State the blood parasite species.
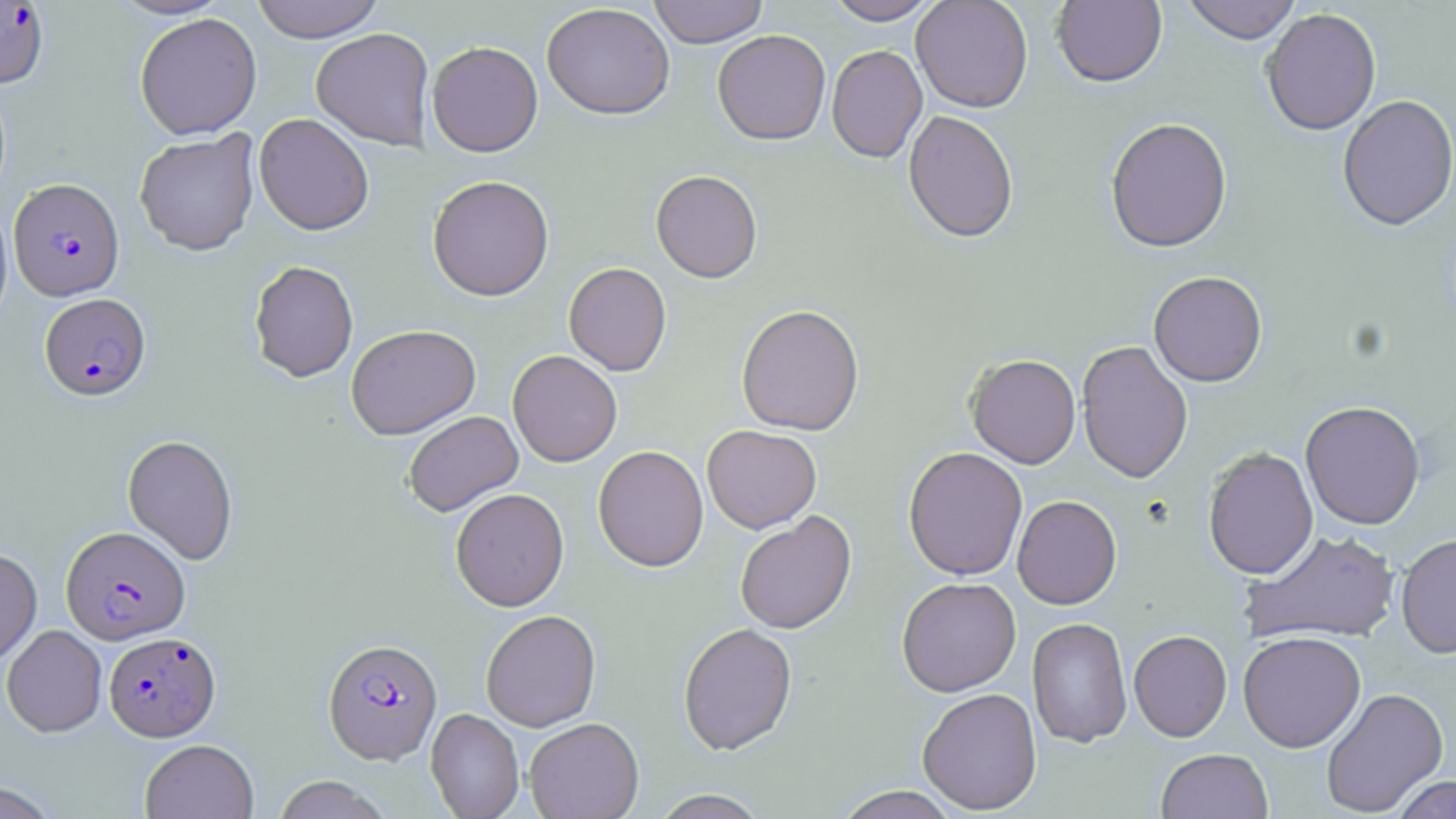

Plasmodium falciparum.

field_of_view: one of a larger specimen
stain: May-Grünwald-Giemsa
modality: light microscopy
preparation: thin blood smear
plasmodium_falciparum_infected_red_blood_cell_locations: 'approximate bounding boxes as named x1/y1/x2/y2 corners in pixels: (x1=0, y1=1, x2=50, y2=88), (x1=8, y1=178, x2=125, y2=300), (x1=39, y1=293, x2=151, y2=400), (x1=61, y1=525, x2=190, y2=644), (x1=104, y1=631, x2=220, y2=741), (x1=323, y1=638, x2=442, y2=764)'
image_size: 1456×819 pixels
uninfected_red_blood_cell_locations: 'approximate bounding boxes as named x1/y1/x2/y2 corners in pixels: (x1=109, y1=0, x2=232, y2=20), (x1=251, y1=0, x2=385, y2=43), (x1=648, y1=0, x2=768, y2=48), (x1=825, y1=0, x2=941, y2=25), (x1=911, y1=0, x2=1033, y2=114), (x1=1051, y1=0, x2=1167, y2=88), (x1=1181, y1=0, x2=1303, y2=45), (x1=541, y1=2, x2=675, y2=120), (x1=1261, y1=9, x2=1382, y2=137), (x1=134, y1=12, x2=262, y2=140), (x1=310, y1=27, x2=434, y2=151), (x1=712, y1=29, x2=831, y2=146), (x1=426, y1=41, x2=543, y2=157), (x1=826, y1=45, x2=927, y2=163), (x1=1337, y1=96, x2=1456, y2=233), (x1=903, y1=110, x2=1019, y2=244), (x1=254, y1=113, x2=374, y2=235), (x1=1105, y1=119, x2=1232, y2=255), (x1=134, y1=130, x2=260, y2=256), (x1=651, y1=169, x2=763, y2=283), (x1=427, y1=174, x2=555, y2=301), (x1=0, y1=198, x2=14, y2=333), (x1=248, y1=260, x2=359, y2=382), (x1=564, y1=262, x2=672, y2=376), (x1=1148, y1=272, x2=1268, y2=387), (x1=736, y1=304, x2=864, y2=436), (x1=345, y1=324, x2=481, y2=439), (x1=1076, y1=340, x2=1193, y2=484), (x1=507, y1=350, x2=622, y2=467), (x1=966, y1=355, x2=1081, y2=469), (x1=1300, y1=401, x2=1425, y2=530), (x1=403, y1=410, x2=523, y2=517), (x1=702, y1=424, x2=822, y2=533), (x1=122, y1=434, x2=239, y2=564), (x1=593, y1=445, x2=708, y2=572), (x1=903, y1=447, x2=1028, y2=581), (x1=1203, y1=447, x2=1318, y2=580), (x1=450, y1=487, x2=569, y2=611), (x1=1012, y1=495, x2=1122, y2=610), (x1=735, y1=512, x2=856, y2=634), (x1=1240, y1=528, x2=1401, y2=647), (x1=1396, y1=533, x2=1455, y2=659), (x1=0, y1=549, x2=42, y2=666), (x1=896, y1=577, x2=1021, y2=697), (x1=481, y1=610, x2=601, y2=731), (x1=1027, y1=617, x2=1133, y2=748), (x1=678, y1=623, x2=798, y2=755), (x1=1, y1=625, x2=107, y2=737), (x1=1129, y1=630, x2=1232, y2=742), (x1=1237, y1=631, x2=1366, y2=752), (x1=917, y1=687, x2=1042, y2=815), (x1=1321, y1=687, x2=1448, y2=817), (x1=425, y1=708, x2=525, y2=819), (x1=524, y1=717, x2=644, y2=819), (x1=139, y1=739, x2=259, y2=819), (x1=1156, y1=747, x2=1273, y2=819), (x1=271, y1=775, x2=392, y2=819), (x1=1390, y1=775, x2=1455, y2=818), (x1=0, y1=780, x2=61, y2=818), (x1=833, y1=786, x2=961, y2=819), (x1=650, y1=789, x2=770, y2=818)'
magnification: 1000x